State which cell type is depicted.
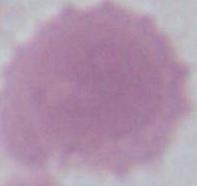

This is an erythrocyte.

modality = photomicrograph
magnification = 1000x